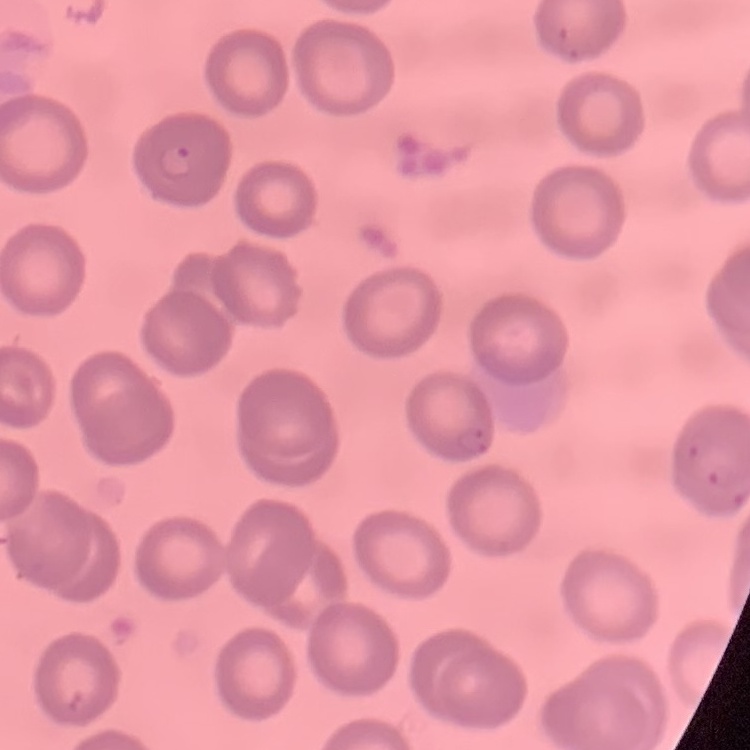
erythrocyte morphology = no rouleaux formation
preparation = thin blood film
stain = Field's or Giemsa
image type = square crop of a larger photomicrograph